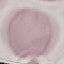
malaria status = uninfected
stain = Giemsa
preparation = thin blood smear
capture = smartphone camera at the microscope eyepiece
image type = cell patch, automatically extracted from a larger field of view and resized to 64 × 64 pixels